State which cell type is depicted.
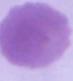

This is an erythrocyte.

Summary:
  - Magnification: 1000x
  - Modality: photomicrograph